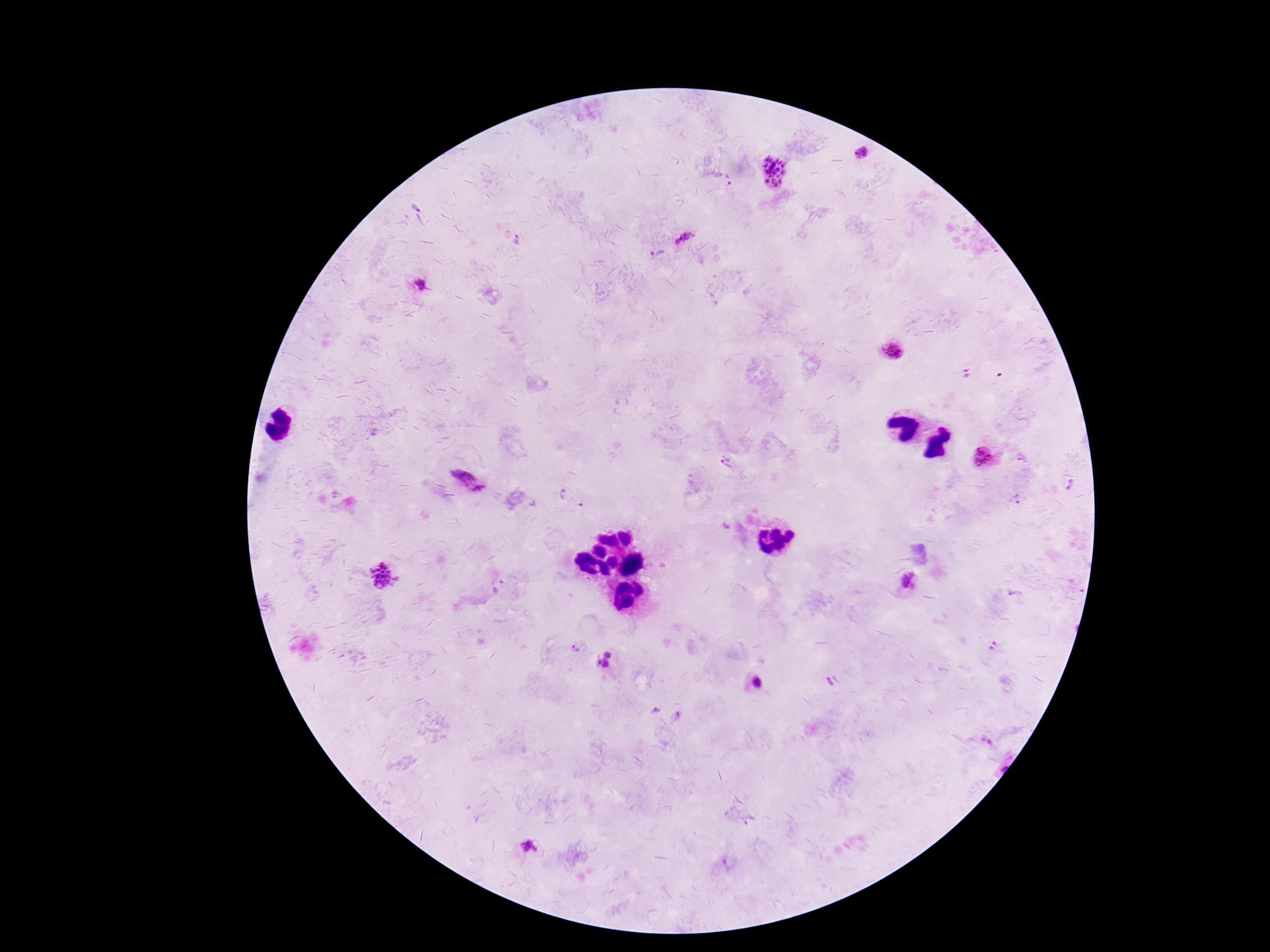 Approximate centers as (x, y) in pixels. Plasmodium parasite locations: (862, 152), (774, 172), (729, 181), (683, 237), (518, 240), (657, 253), (420, 284), (892, 351), (966, 375), (1023, 457), (985, 459), (725, 462), (468, 480), (1070, 484), (570, 497), (1018, 499), (386, 575), (908, 581), (1013, 593), (993, 646), (576, 648), (608, 654), (598, 662), (607, 664), (830, 682), (756, 683), (655, 711), (677, 713), (529, 846). Image is 1270×952 pixels. Single field of view. Patient malaria status: infected. Photographed through the microscope eyepiece with a smartphone camera. 100x magnification. Giemsa-stained preparation. Thick peripheral-blood smear.